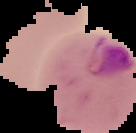

Image is 136×133 pixels. The area outside the segmented cell region is set to black. Result: Plasmodium parasites detected. From a thin blood smear.